Outline each blood parasite and name the species.
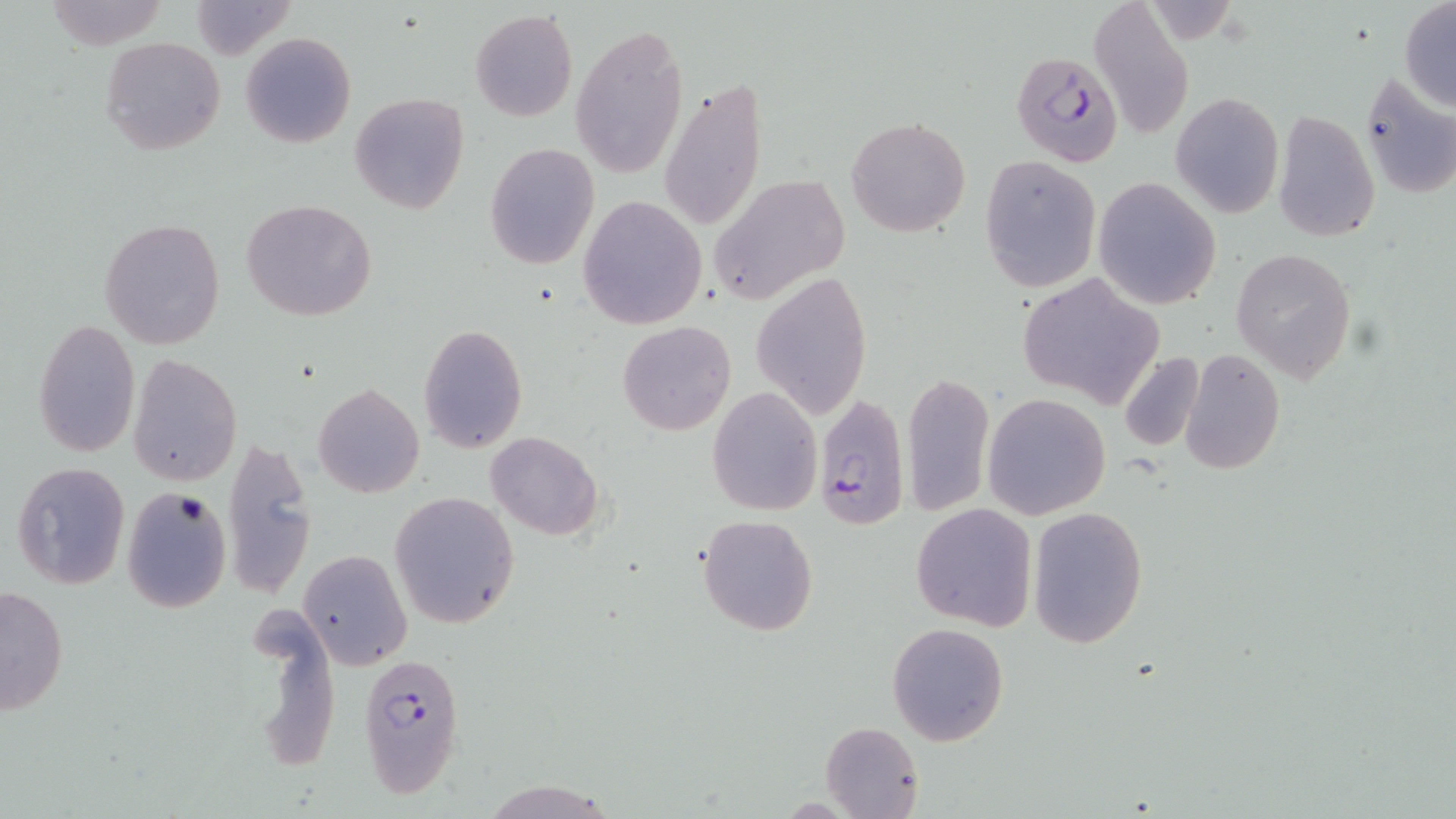

Approximate bounding boxes as (x1,y1)-(x2,y2) corner pairs in pixels.
Plasmodium falciparum-infected red blood cells: (1011,49)-(1123,167), (814,393)-(908,532), (359,649)-(464,799).
No Plasmodium ovale, Plasmodium malariae, Plasmodium vivax, Babesia divergens, or Trypanosoma brucei observed.

{
  "slide_level_diagnosis": "Plasmodium falciparum",
  "field_of_view": "one of a larger specimen",
  "preparation": "thin blood smear",
  "modality": "optical microscopy",
  "uninfected_red_blood_cell_locations": "approximate bounding boxes as (x1,y1)-(x2,y2) corner pairs in pixels: (187,1)-(298,62), (1088,1)-(1195,139), (1399,3)-(1456,111), (468,9)-(578,123), (573,25)-(689,179), (241,33)-(355,148), (100,36)-(225,156), (1356,72)-(1456,202), (659,75)-(766,234), (350,92)-(469,214), (1171,92)-(1284,218), (1272,110)-(1381,242), (846,116)-(969,238), (484,144)-(599,269), (979,154)-(1102,293), (708,172)-(848,306), (1093,177)-(1222,310), (579,195)-(707,330), (241,200)-(376,320), (99,218)-(225,349), (1231,249)-(1356,383), (752,270)-(871,418), (1018,272)-(1161,410), (32,319)-(140,458), (617,321)-(736,435), (417,323)-(528,453), (1179,348)-(1284,476), (1116,351)-(1205,453), (129,354)-(242,487), (902,371)-(994,517), (313,384)-(424,499), (707,386)-(822,515), (982,394)-(1111,519), (485,431)-(603,541), (222,435)-(317,600), (11,462)-(129,590), (121,487)-(232,612), (390,491)-(519,629), (910,503)-(1038,632), (1026,506)-(1148,648), (698,513)-(818,637), (297,549)-(411,670), (1,585)-(69,716), (254,609)-(343,773), (887,622)-(1009,746), (819,720)-(924,819)",
  "stain": "May-Grünwald-Giemsa",
  "magnification": "1000x",
  "image_size": "1456×819 pixels"
}